Give the position of every Plasmodium parasite visible.
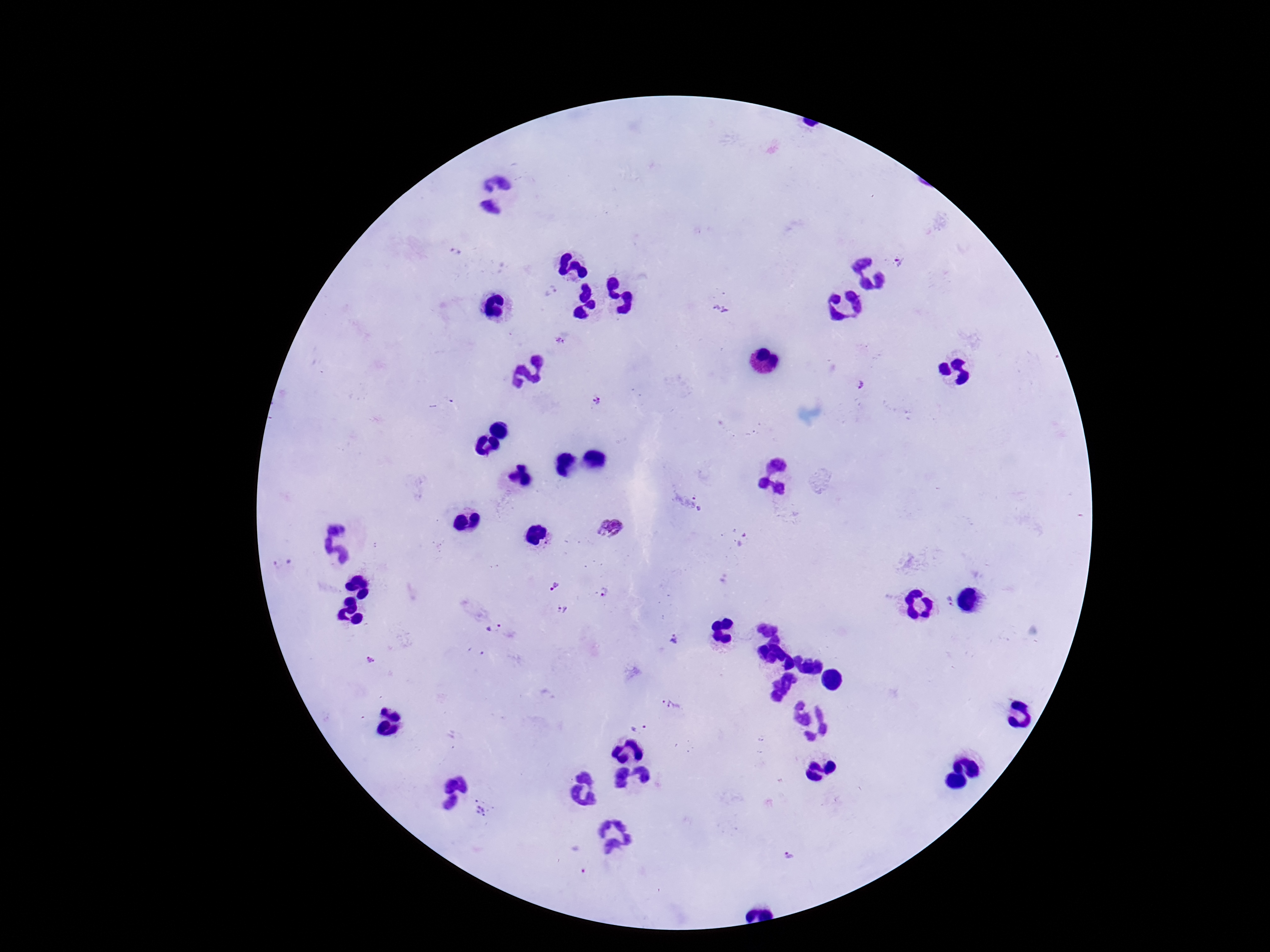
Approximate centers as [x, y] in pixels.
Plasmodium parasites: [454, 251], [899, 260], [550, 291], [721, 306], [561, 342], [861, 384], [597, 399], [700, 502], [613, 527], [282, 563], [556, 584], [604, 591], [947, 600], [563, 608], [492, 629], [677, 639], [377, 659], [669, 705], [640, 726], [484, 809], [576, 858], [792, 858].

Summary:
  - Preparation: thick blood film
  - Stain: Giemsa
  - Image size: 1270×952 pixels
  - Magnification: 100x
  - Field of view: single
  - Patient malaria status: positive
  - Capture: smartphone camera through the microscope eyepiece